Give the position of every Plasmodium parasite.
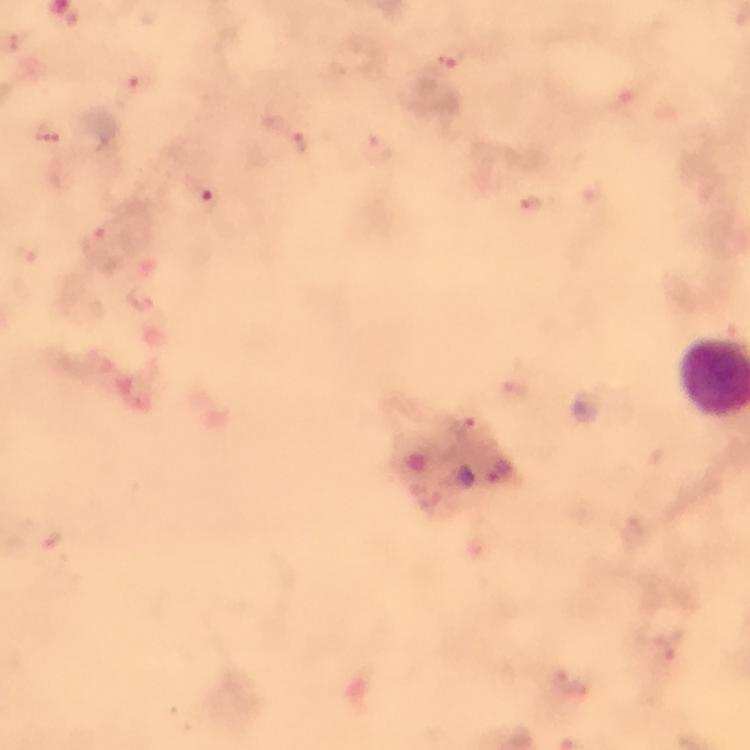

Approximate centers as {x, y} in pixels.
Plasmodium parasites: {450, 56}, {126, 89}, {49, 129}, {298, 144}, {378, 150}, {204, 194}, {529, 204}, {94, 239}, {471, 422}, {51, 540}, {667, 651}, {573, 682}.

{
  "image_size": "750×750 pixels",
  "cropped_from": "one field of view",
  "capture": "smartphone photograph through a microscope",
  "context": "from a diagnostic examination for malaria",
  "stain": "Giemsa",
  "immersion_oil": "applied",
  "magnification": "100x",
  "preparation": "thick blood smear"
}